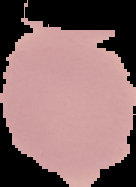

Summary:
  - Image type: segmented cell region with the area outside set to black
  - Result: no malaria parasites detected
  - Image size: 136×187 pixels
  - Preparation: thin blood film